Classify this cell by malaria status.
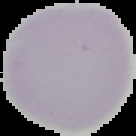
Uninfected.

Summary:
  - Image size: 136×136 pixels
  - Image type: segmented cell region with the area outside set to black
  - Preparation: thin blood smear